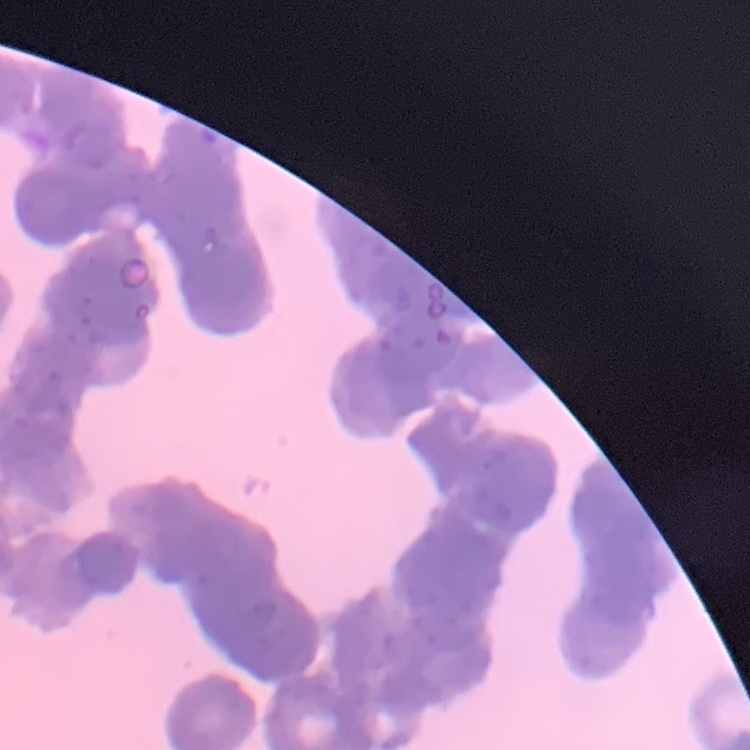

red_blood_cell_morphology: rouleaux formation
preparation: thin blood film
image_type: square crop of a larger photomicrograph
stain: Field's or Giemsa